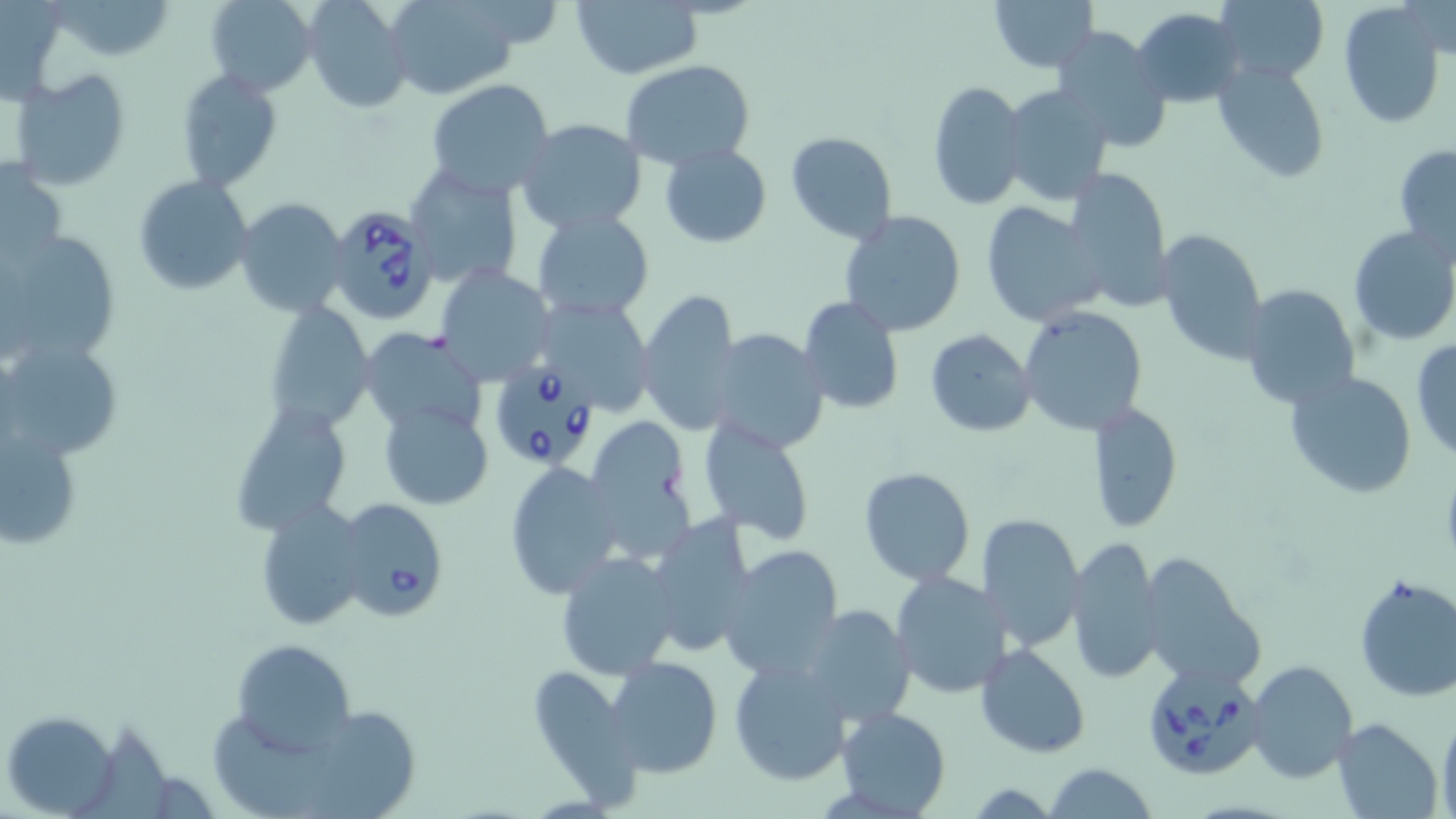
slide-level diagnosis = Babesia divergens
image size = 1456×819 pixels
magnification = 1000x
stain = May-Grünwald-Giemsa
field of view = single
Babesia divergens-infected red blood cell locations = approximate bounding boxes as [x1, y1, x2, y2] in pixels: [325, 203, 441, 326], [492, 362, 599, 468], [335, 498, 449, 623], [1138, 658, 1268, 781]
modality = light microscopy
uninfected red blood cell locations = approximate bounding boxes as [x1, y1, x2, y2] in pixels: [54, 0, 171, 61], [204, 0, 318, 96], [301, 0, 411, 113], [988, 0, 1097, 73], [1212, 0, 1330, 86], [387, 1, 518, 100], [571, 1, 702, 79], [1338, 2, 1445, 126], [1132, 8, 1244, 108], [1047, 25, 1172, 153], [619, 60, 754, 170], [1211, 60, 1332, 186], [12, 69, 131, 190], [175, 69, 281, 191], [426, 79, 555, 197], [927, 79, 1030, 212], [1001, 84, 1115, 206], [514, 119, 649, 236], [786, 131, 897, 243], [1394, 142, 1456, 262], [658, 143, 772, 248], [0, 162, 67, 268], [403, 163, 524, 290], [1062, 167, 1173, 309], [133, 174, 253, 295], [236, 198, 348, 318], [979, 201, 1106, 327], [530, 210, 655, 322], [838, 210, 966, 337], [3, 226, 118, 364], [1157, 226, 1267, 364], [1348, 226, 1456, 347], [435, 264, 556, 385], [1241, 285, 1360, 411], [635, 286, 744, 439], [531, 294, 658, 414], [795, 297, 904, 415], [264, 298, 377, 433], [1018, 306, 1149, 436], [709, 326, 830, 453], [360, 328, 489, 439], [923, 328, 1036, 437], [1410, 336, 1456, 461], [3, 337, 121, 463], [1285, 370, 1418, 500], [228, 399, 355, 535], [378, 400, 493, 510], [1087, 400, 1184, 533], [2, 417, 84, 556], [583, 418, 695, 557], [697, 419, 816, 544], [506, 461, 625, 599], [859, 466, 976, 586], [255, 501, 370, 632], [977, 513, 1084, 652], [646, 514, 757, 657], [1065, 539, 1163, 682], [720, 544, 845, 680], [554, 551, 682, 680], [1138, 552, 1265, 691], [890, 569, 1011, 699], [1353, 573, 1456, 703], [801, 604, 915, 726], [230, 638, 356, 754], [976, 642, 1090, 757], [606, 655, 723, 776], [728, 655, 854, 786], [1247, 660, 1358, 783], [534, 665, 644, 815], [3, 708, 118, 815], [836, 708, 952, 818], [311, 712, 418, 819], [1439, 712, 1456, 819], [1334, 718, 1443, 816], [213, 720, 322, 819], [83, 724, 175, 819], [1042, 763, 1158, 819]
preparation = thin blood smear